Identify the preparation type.
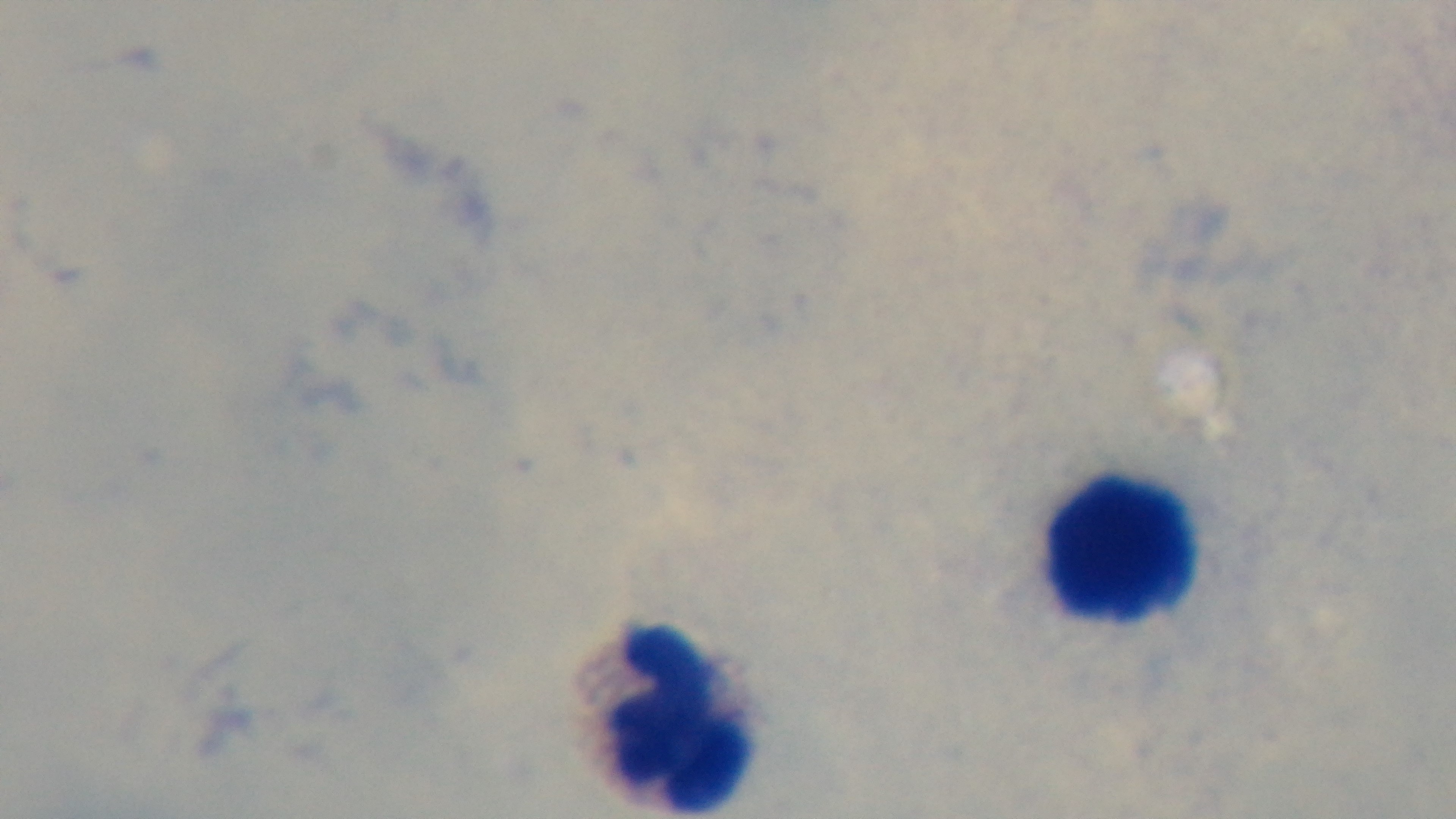

A thick smear.

{
  "stain": "Giemsa",
  "malaria_status": "uninfected",
  "capture": "mounted 4K digital camera",
  "field_of_view": "one from the slide",
  "objective": "100x oil immersion",
  "modality": "light microscopy"
}